Locate and identify every blood parasite.
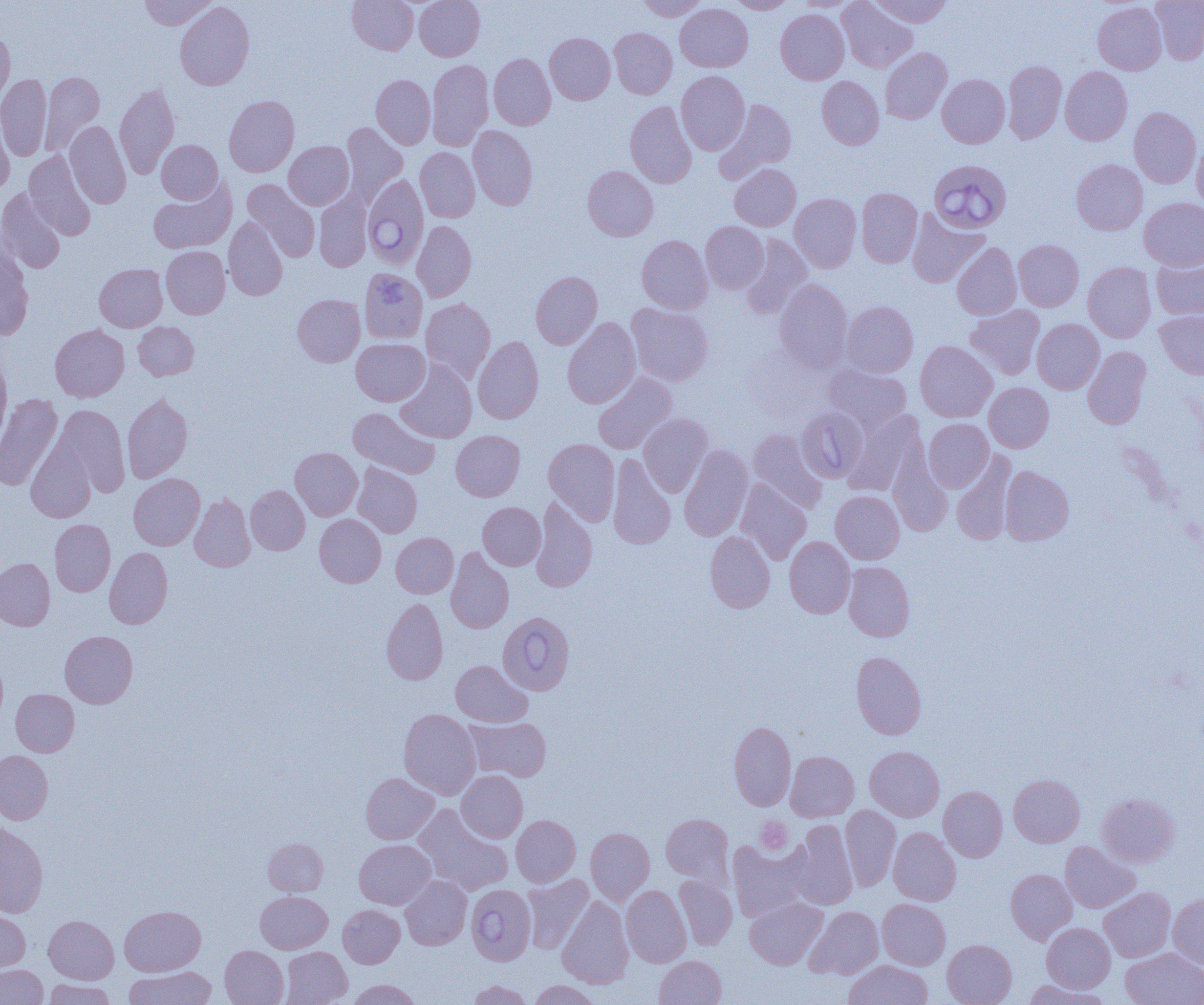
Approximate bounding boxes as (x1,y1)-(x2,y2) corner pairs in pixels.
Babesia divergens-infected red blood cells: (929,159)-(1011,233), (362,173)-(429,269), (497,612)-(575,694), (466,884)-(536,965).
No Plasmodium falciparum, Plasmodium ovale, Plasmodium malariae, Plasmodium vivax, or Trypanosoma brucei observed.

Summary:
  - Uninfected red blood cell locations: (139,0)-(218,30), (347,0)-(418,55), (414,0)-(484,60), (638,0)-(708,20), (729,0)-(794,14), (793,0)-(861,11), (837,0)-(917,73), (870,0)-(952,27), (1151,0)-(1204,64), (175,2)-(255,90), (1093,2)-(1166,75), (675,3)-(753,72), (775,10)-(849,84), (609,27)-(677,99), (0,28)-(15,106), (545,33)-(615,104), (880,47)-(952,124), (489,53)-(556,130), (427,60)-(494,150), (1003,60)-(1066,143), (1060,66)-(1132,145), (41,71)-(104,152), (676,71)-(749,155), (1,74)-(52,161), (937,74)-(1009,148), (371,75)-(435,149), (817,76)-(884,149), (114,84)-(179,179), (224,95)-(299,177), (718,99)-(796,179), (625,101)-(697,188), (1129,107)-(1201,188), (0,114)-(14,194), (65,121)-(131,208), (341,122)-(408,204), (468,126)-(537,210), (1192,138)-(1204,211), (156,140)-(223,204), (284,141)-(354,209), (415,147)-(480,222), (24,151)-(96,241), (1071,159)-(1148,235), (730,164)-(800,231), (582,166)-(658,241), (149,179)-(236,253), (242,179)-(320,263), (0,188)-(67,274), (856,188)-(922,268), (314,192)-(371,271), (790,194)-(861,272), (1139,198)-(1204,270), (907,210)-(988,287), (223,216)-(288,300), (412,221)-(476,302), (700,221)-(769,293), (637,235)-(712,314), (740,235)-(813,319), (1014,240)-(1084,311), (951,242)-(1022,319), (161,246)-(230,319), (0,247)-(33,341), (1152,256)-(1204,321), (1083,262)-(1156,342), (94,264)-(167,331), (363,270)-(420,345), (531,271)-(602,349), (774,279)-(853,372), (292,294)-(365,367), (420,298)-(495,383), (840,301)-(918,378), (626,303)-(714,386), (965,305)-(1044,379), (1155,310)-(1204,379), (562,318)-(641,408), (1032,318)-(1104,394), (133,321)-(199,380), (50,324)-(129,401), (473,337)-(543,423), (351,338)-(429,406), (915,341)-(997,422), (1083,346)-(1151,429), (0,351)-(11,448), (395,360)-(477,443), (823,363)-(911,433), (592,371)-(677,454), (984,382)-(1054,452), (0,393)-(63,491), (122,393)-(193,483), (53,405)-(130,496), (348,407)-(439,478), (796,407)-(869,483), (843,410)-(924,496), (639,413)-(713,496), (924,418)-(993,492), (748,428)-(827,513), (451,430)-(525,501), (26,438)-(97,522), (544,438)-(620,525), (679,445)-(753,541), (290,448)-(362,520), (888,449)-(952,536), (951,451)-(1016,545), (607,454)-(676,550), (353,462)-(422,538), (1000,466)-(1074,545), (128,473)-(205,550), (735,479)-(811,565), (246,485)-(310,555), (830,491)-(904,564), (189,494)-(255,572), (531,497)-(597,593), (478,502)-(546,570), (314,514)-(386,587), (50,519)-(115,596), (705,531)-(775,613), (391,532)-(458,597), (784,536)-(855,618), (104,547)-(173,629), (446,547)-(513,633), (0,558)-(55,631), (844,562)-(914,641), (381,598)-(448,685), (60,630)-(137,708), (851,651)-(926,739), (0,656)-(8,725), (451,660)-(532,727), (10,689)-(79,756), (398,709)-(480,799), (464,717)-(551,781), (729,721)-(796,811), (865,746)-(944,821), (0,750)-(53,824), (786,751)-(859,821), (456,770)-(527,842), (361,773)-(439,844), (1009,774)-(1084,847), (939,786)-(1007,861), (1097,792)-(1180,867), (840,804)-(901,891), (413,805)-(513,895), (661,813)-(733,884), (511,815)-(580,886), (790,820)-(858,909), (0,823)-(48,917), (888,827)-(961,906), (586,828)-(654,906), (263,838)-(328,895), (354,839)-(435,909), (726,840)-(812,921), (1060,842)-(1140,912), (1005,869)-(1076,944), (522,874)-(593,954), (675,874)-(737,949), (400,876)-(471,950), (621,885)-(691,967), (1099,887)-(1175,961), (255,891)-(333,953), (1168,894)-(1204,969), (557,895)-(633,988), (745,897)-(827,969), (877,899)-(950,969), (338,904)-(404,968), (119,905)-(205,976), (805,906)-(883,979), (0,909)-(30,972), (44,915)-(118,983), (1042,923)-(1115,992), (942,939)-(1017,1005), (220,946)-(288,1005), (281,947)-(351,1005), (1121,948)-(1204,1005), (654,955)-(726,1005), (844,960)-(932,1005), (0,965)-(48,1004), (124,966)-(216,1005), (44,979)-(116,1004), (348,979)-(421,1005), (467,980)-(532,1005), (530,980)-(600,1005), (1024,981)-(1113,1005)
  - Platelet locations: (756,816)-(793,854)
  - Slide-level diagnosis: Babesia divergens
  - Modality: optical microscopy
  - Preparation: thin blood film
  - Magnification: 1000x
  - Field of view: single
  - Image size: 1204×1005 pixels